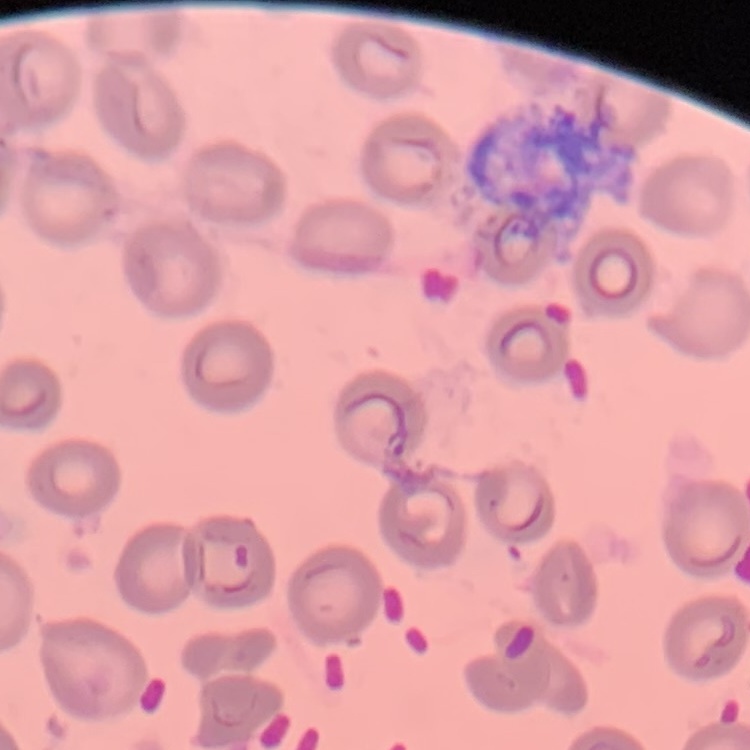
Summary:
  - Erythrocyte morphology: no rouleaux formation
  - Image type: square crop of a larger photomicrograph
  - Preparation: thin blood film
  - Stain: Field's or Giemsa